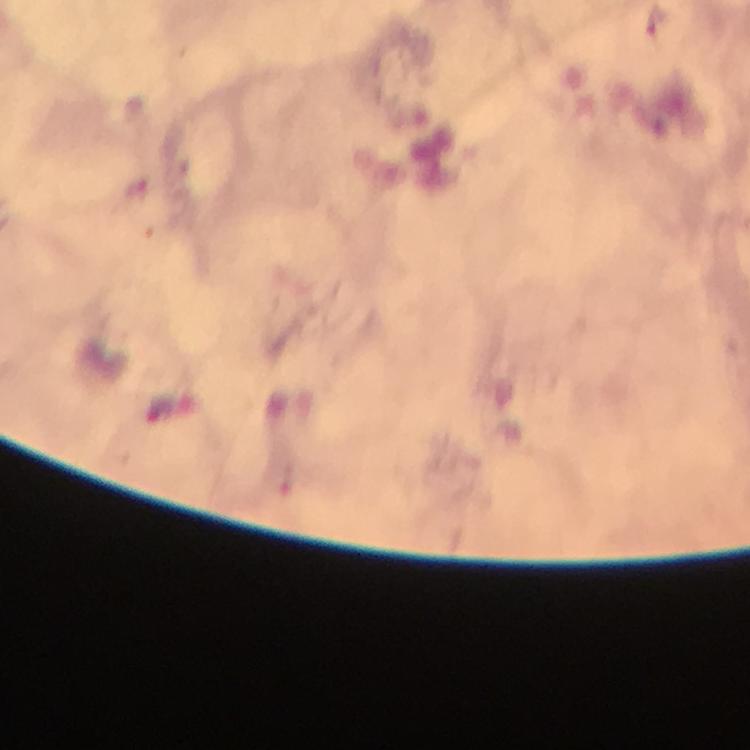 Approximate centers as {x, y} in pixels. Malaria parasite locations: {139, 187}. Smartphone photograph taken through a microscope. Giemsa stain. At 100x magnification. From a diagnostic examination for malaria. Immersion oil was used. Thick smear. Image is 750×750 pixels. A crop from one field of view.